Report the malaria status of this cell.
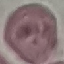
Uninfected.

Giemsa stain. Thin smear of blood. Cell patch, automatically extracted from a larger field of view and resized to 64 × 64 pixels. Acquired by smartphone through the microscope eyepiece.